Outline Plasmodium falciparum parasites and classify them by life-cycle stage.
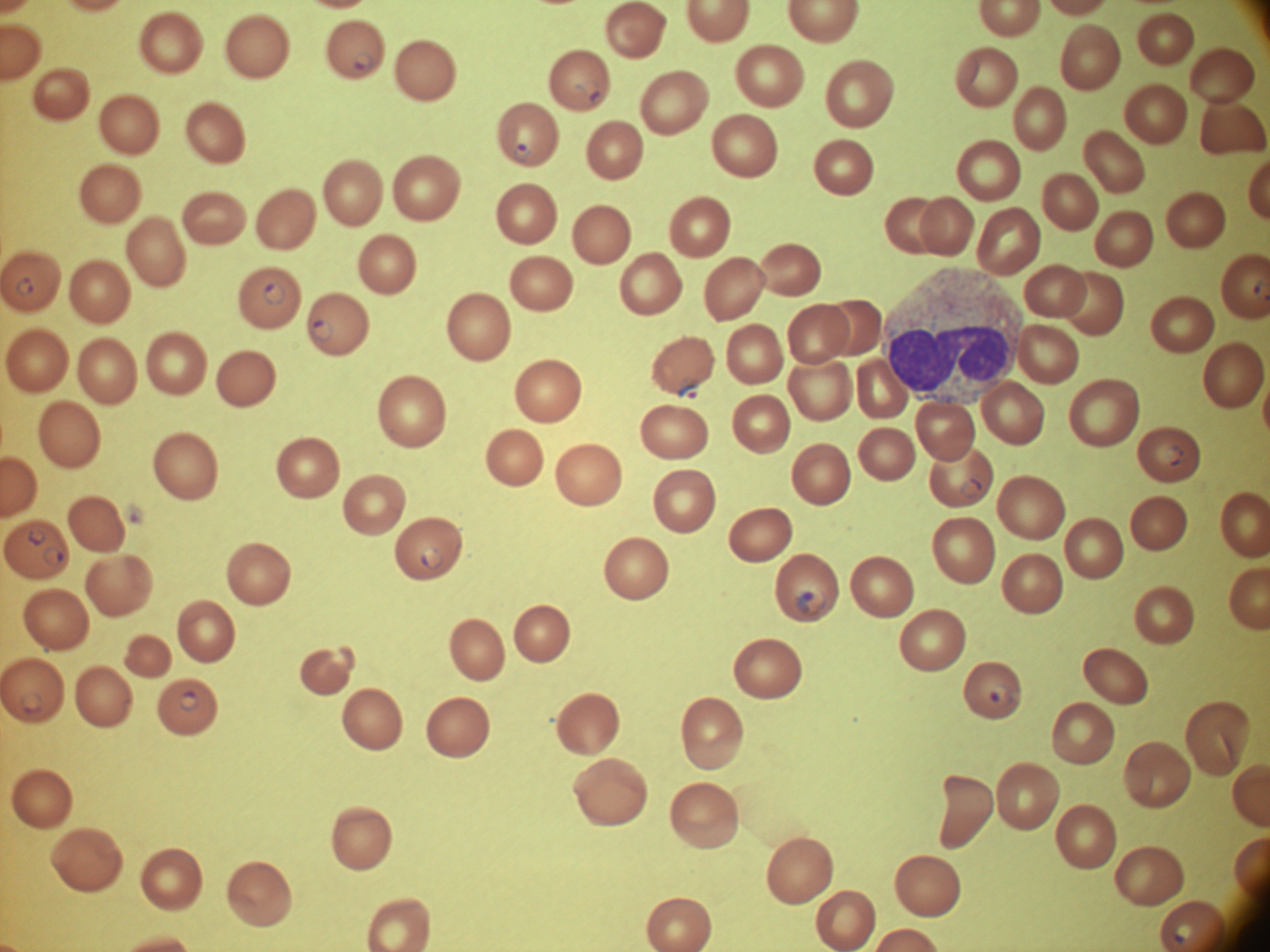

Approximate bounding boxes as (x1, y1, x2, y2) in pixels, from the source annotation, which is not necessarily exhaustive.
Ring forms: (352, 51, 375, 72), (578, 80, 602, 100), (513, 143, 531, 164), (16, 276, 34, 296), (262, 281, 287, 306), (311, 318, 334, 343), (677, 379, 702, 401), (1163, 445, 1184, 466), (960, 477, 982, 500), (28, 528, 47, 547), (43, 546, 64, 567), (419, 547, 444, 571), (793, 585, 827, 617), (989, 684, 1014, 708), (20, 690, 45, 715), (179, 690, 199, 712), (1172, 921, 1195, 943).

Summary:
  - Stain: Giemsa
  - Magnification: 100x
  - Microscope: Leica DM2000 with built-in camera
  - Species: Plasmodium falciparum
  - Preparation: thin blood smear
  - Field of view: one from this slide
  - Image size: 1270×952 pixels